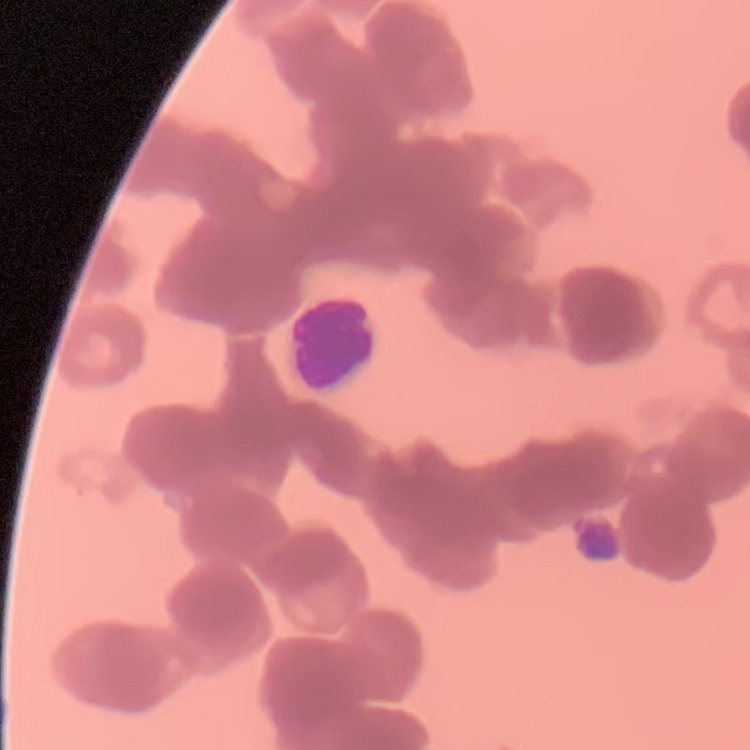

Summary:
  - Red blood cell morphology: rouleaux formation
  - Image type: square crop of a larger photomicrograph
  - Preparation: thin blood smear
  - Stain: Field's or Giemsa